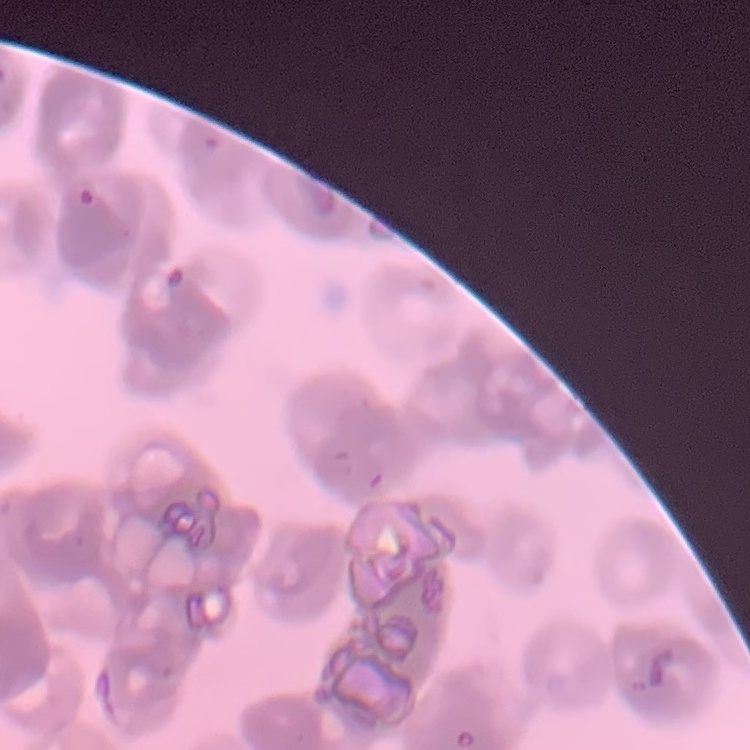 The red blood cells exhibit rouleaux formation. Thin peripheral smear. Square crop of a larger photomicrograph. Field's or Giemsa stain.